Locate every Plasmodium falciparum-infected red blood cell.
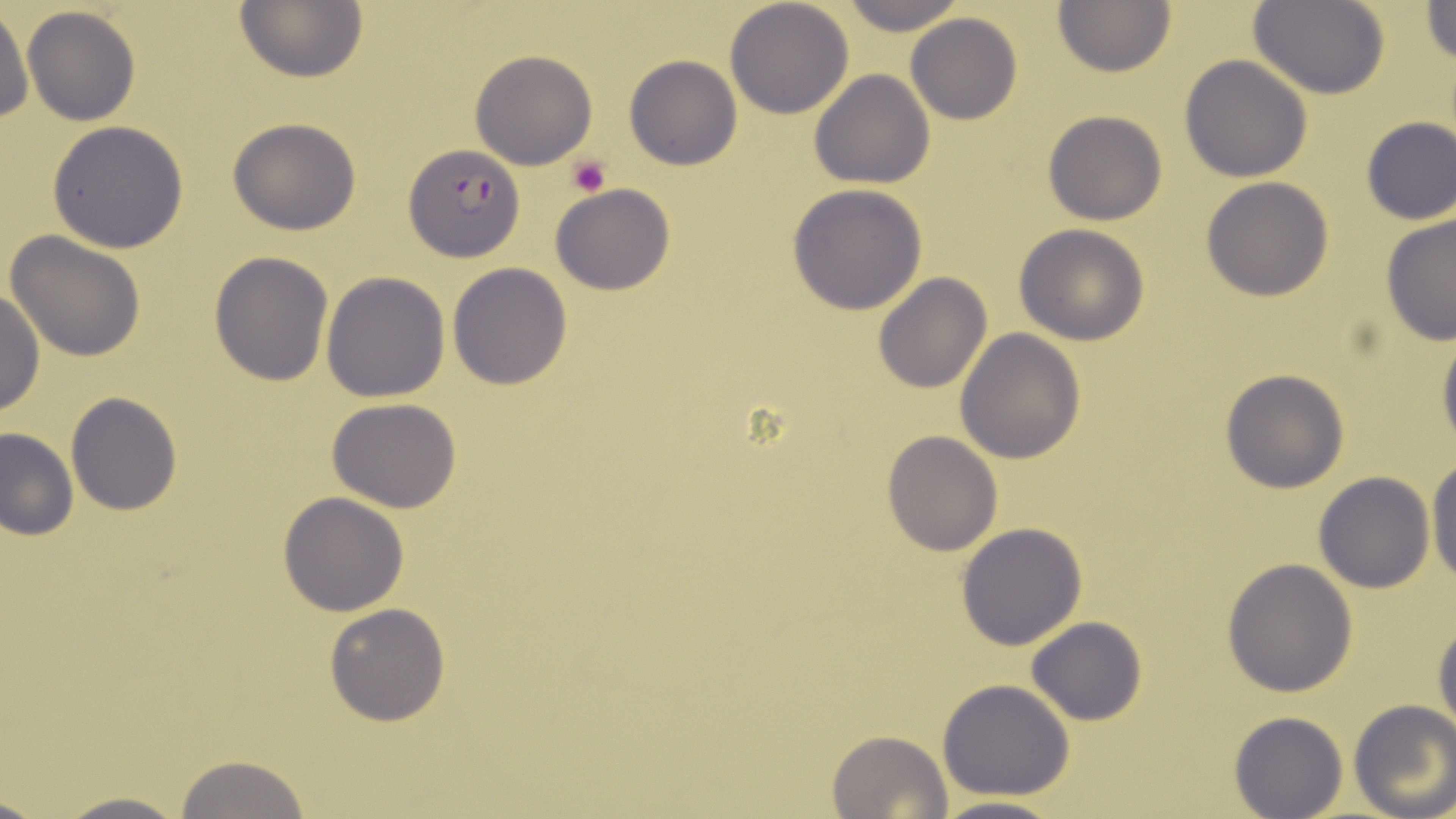
Approximate bounding boxes as (x1, y1, x2, y2) in pixels.
Plasmodium falciparum-infected red blood cells: (406, 144, 524, 263).

Summary:
  - Platelet locations: (566, 156, 611, 198)
  - Uninfected red blood cell locations: (234, 0, 369, 84), (724, 0, 854, 118), (836, 0, 967, 31), (1053, 0, 1176, 75), (1251, 0, 1390, 98), (1422, 0, 1456, 66), (0, 6, 33, 126), (21, 6, 141, 126), (905, 13, 1024, 123), (469, 51, 598, 169), (1179, 54, 1313, 182), (624, 56, 741, 170), (809, 69, 935, 189), (1044, 109, 1166, 224), (1359, 115, 1454, 225), (227, 117, 362, 235), (47, 120, 191, 252), (1201, 176, 1335, 301), (551, 183, 674, 294), (787, 184, 929, 316), (1379, 212, 1456, 344), (1014, 224, 1150, 346), (4, 230, 148, 361), (209, 252, 334, 386), (447, 263, 573, 391), (321, 271, 450, 401), (872, 275, 992, 394), (0, 288, 43, 418), (955, 328, 1085, 464), (1436, 329, 1456, 455), (1220, 369, 1349, 493), (66, 392, 181, 515), (326, 398, 463, 513), (0, 427, 77, 540), (881, 430, 1002, 556), (1427, 460, 1456, 593), (1313, 471, 1435, 592), (279, 493, 408, 616), (955, 522, 1087, 650), (1222, 558, 1357, 697), (323, 602, 451, 725), (1433, 614, 1456, 740), (1027, 615, 1146, 725), (937, 679, 1076, 801), (1349, 700, 1456, 818), (1229, 711, 1347, 818), (828, 729, 951, 818), (173, 754, 315, 818), (47, 791, 192, 819), (928, 794, 1070, 819)
  - Slide-level diagnosis: Plasmodium falciparum
  - Field of view: one of a larger specimen
  - Modality: optical microscopy
  - Magnification: 1000x
  - Preparation: thin blood film
  - Image size: 1456×819 pixels
  - Stain: May-Grünwald-Giemsa